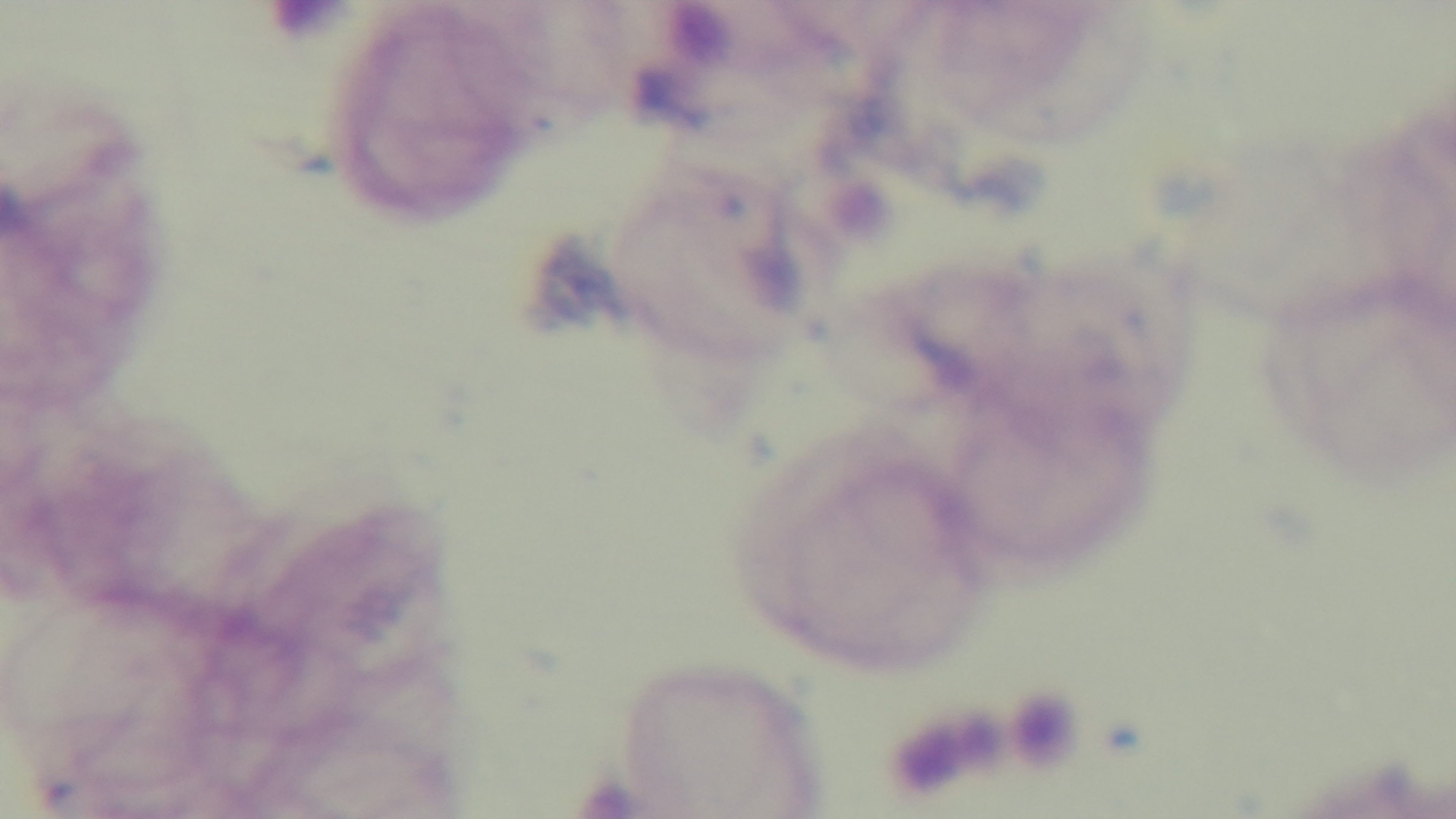
Preparation: thick. Malaria status: negative. Oil-immersion objective, 100x. Captured with a mounted 4K digital camera. Light microscopy. Single field of view. Giemsa-stained.